Locate every Plasmodium parasite.
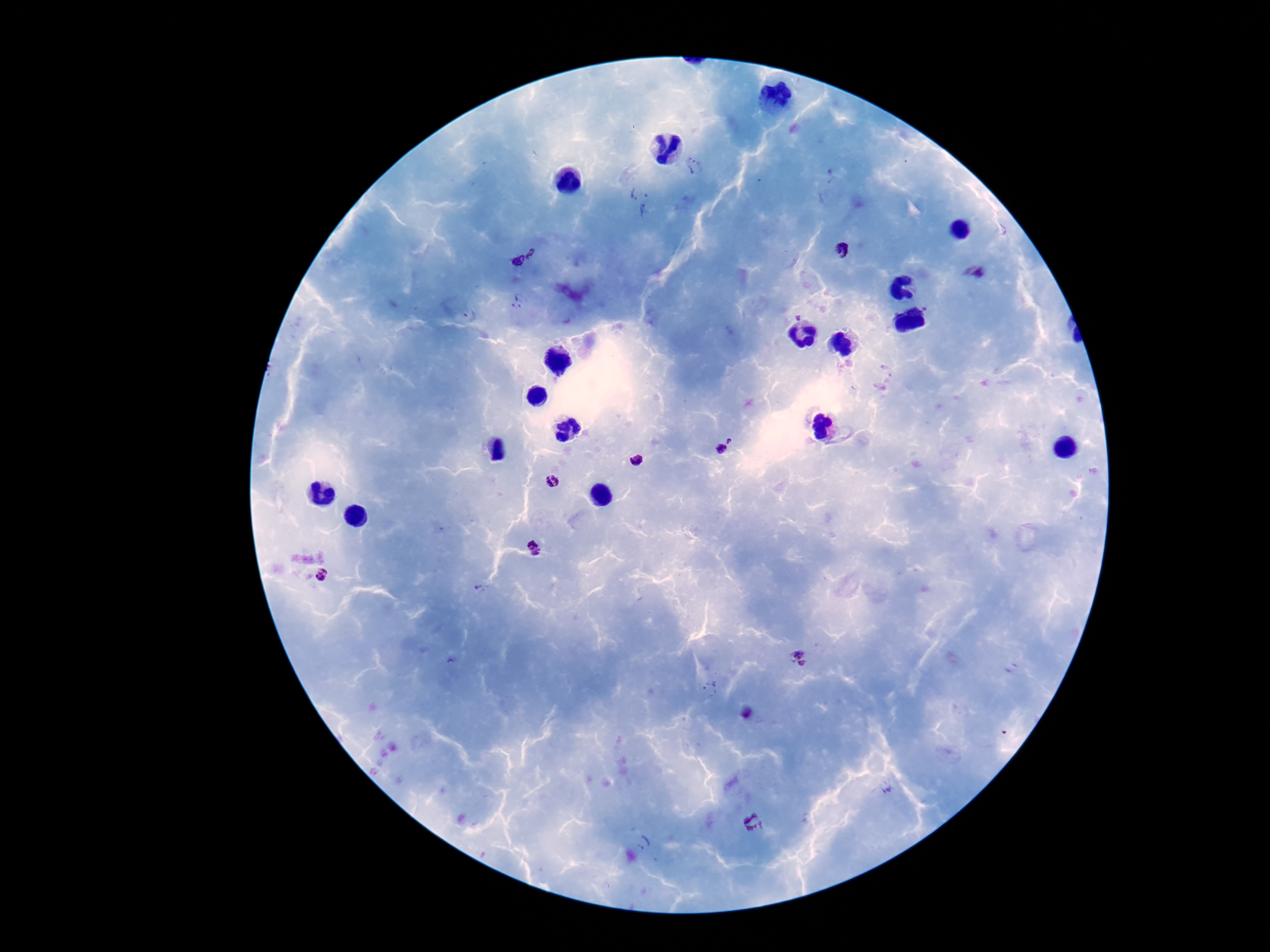
Approximate centers as {x, y} in pixels.
Plasmodium parasites: {695, 166}, {639, 192}, {645, 212}, {842, 250}, {533, 252}, {518, 262}, {978, 273}, {519, 300}, {470, 315}, {731, 439}, {722, 448}, {635, 461}, {552, 481}, {534, 549}, {321, 576}, {799, 656}, {710, 689}, {748, 714}, {753, 822}, {644, 843}.

100x magnification. Image is 1270×952 pixels. Giemsa-stained preparation. Single field of view. Patient malaria status: positive. Photographed through the microscope eyepiece with a smartphone camera. Thick peripheral-blood smear.